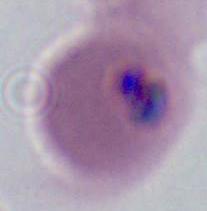
Micrograph. Captured at either 400x or 1000x magnification. A Plasmodium parasite is seen.